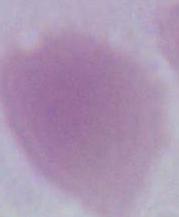
Micrograph. 1000x magnification. A red blood cell is shown.